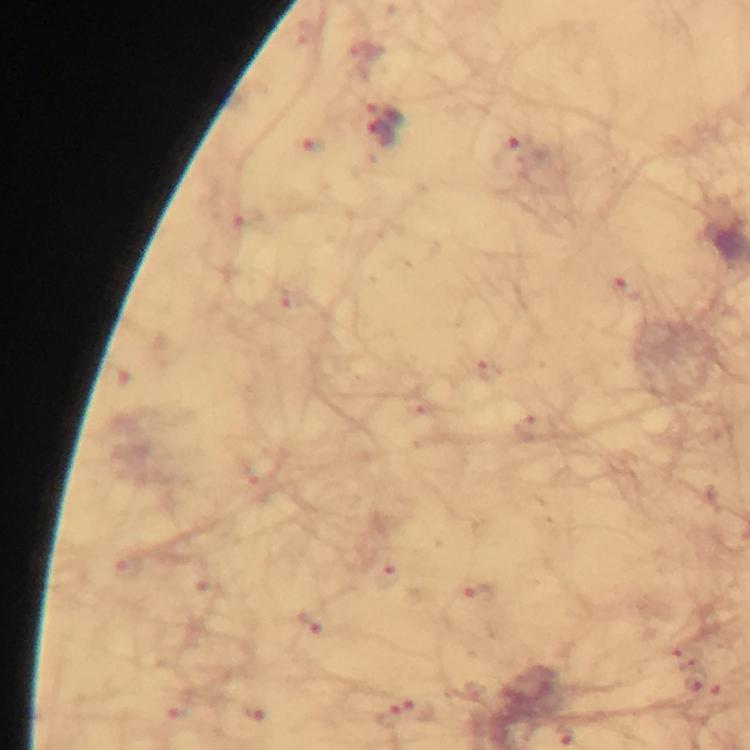
Approximate object centers, in pixels from the top-left corner.
Summary:
  - Malaria parasite locations: (x=386, y=113), (x=375, y=133), (x=513, y=147)
  - Magnification: 100x
  - Preparation: thick blood smear
  - Cropped from: a single field of view
  - Image size: 750×750 pixels
  - Stain: Giemsa
  - Immersion oil: used
  - Capture: smartphone camera through the microscope
  - Context: from a diagnostic examination for malaria